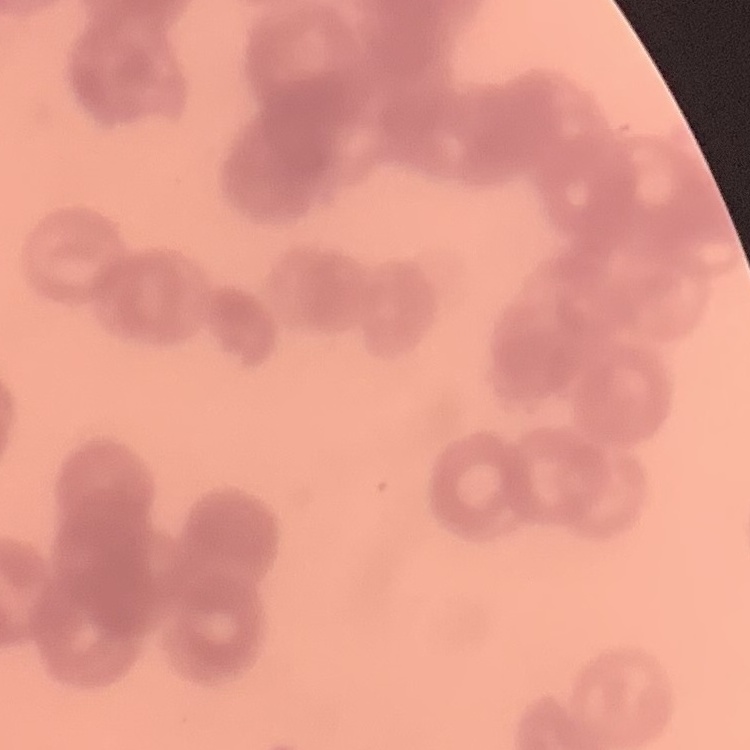 The red blood cells exhibit rouleaux formation. Square crop of a larger photomicrograph. Thin peripheral smear. Field's or Giemsa stain.